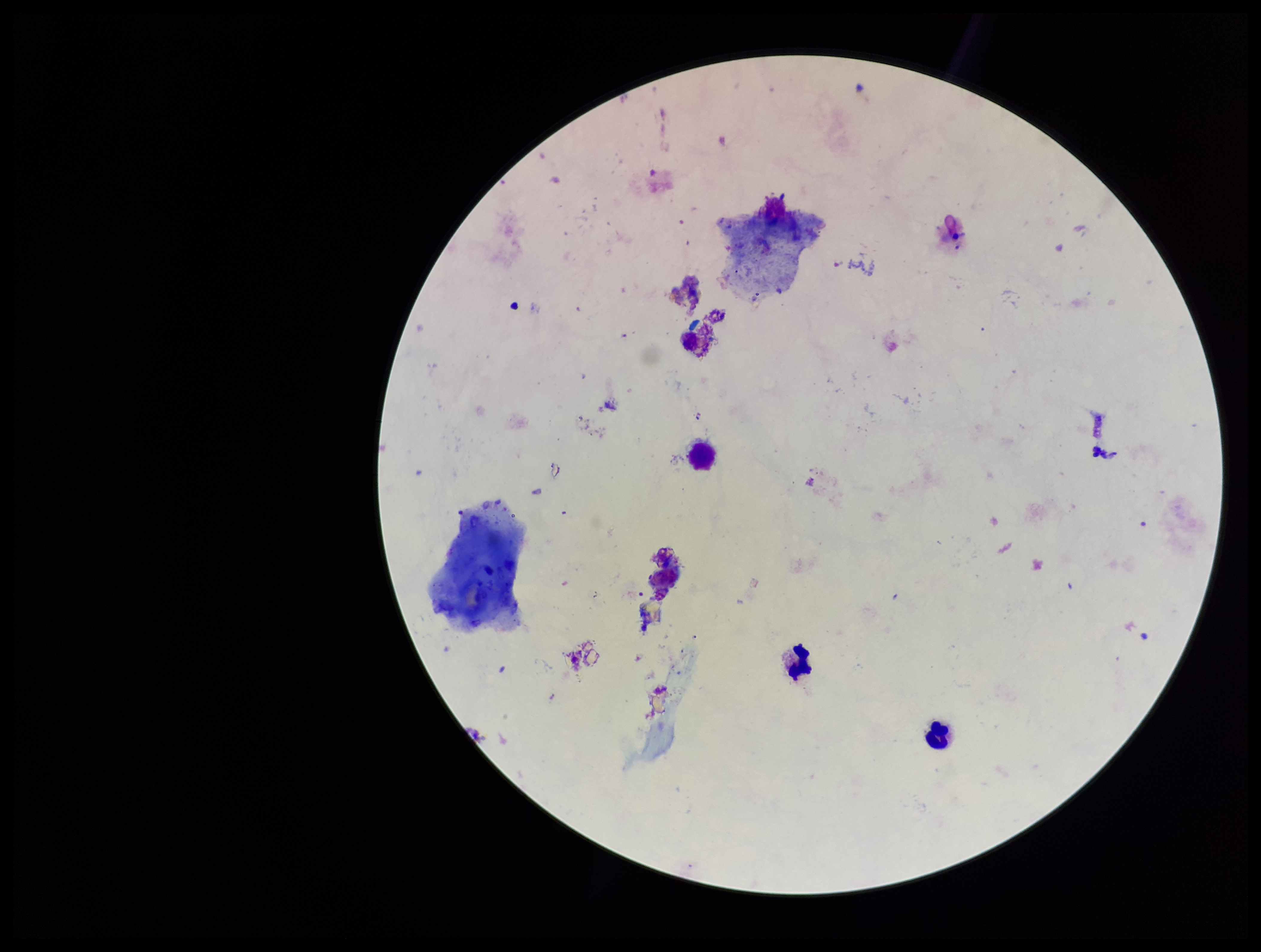

Summary:
  - Capture: smartphone photograph through the microscope eyepiece
  - Field of view: one from this slide
  - Preparation: thick
  - Parasite count: 0
  - Image size: 1261×952 pixels
  - Stain: Giemsa
  - Patient malaria status: negative
  - Plasmodium parasites: none detected
  - Leukocyte count: 4